Give the position of every leukocyte visible.
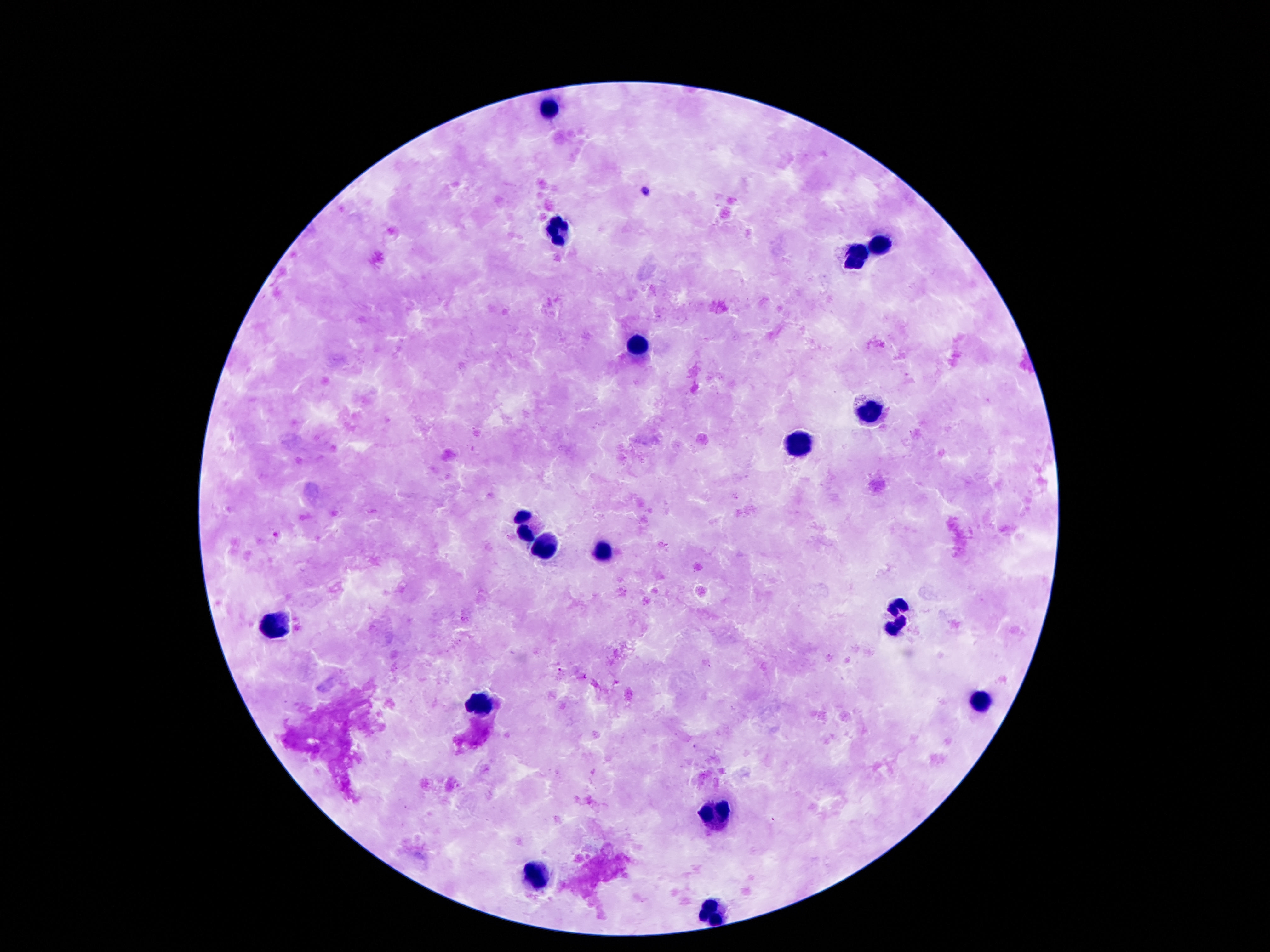

Approximate centers as (x, y) in pixels.
Leukocytes: (549, 107), (555, 230), (883, 246), (858, 253), (639, 347), (868, 414), (796, 446), (528, 527), (549, 546), (602, 548), (897, 621), (274, 623), (979, 699), (479, 703), (713, 813), (536, 875), (710, 914).

magnification: 100x
patient_malaria_status: not infected
stain: Giemsa
image_size: 1270×952 pixels
capture: smartphone camera through the microscope eyepiece
preparation: thick blood film
field_of_view: one from this slide